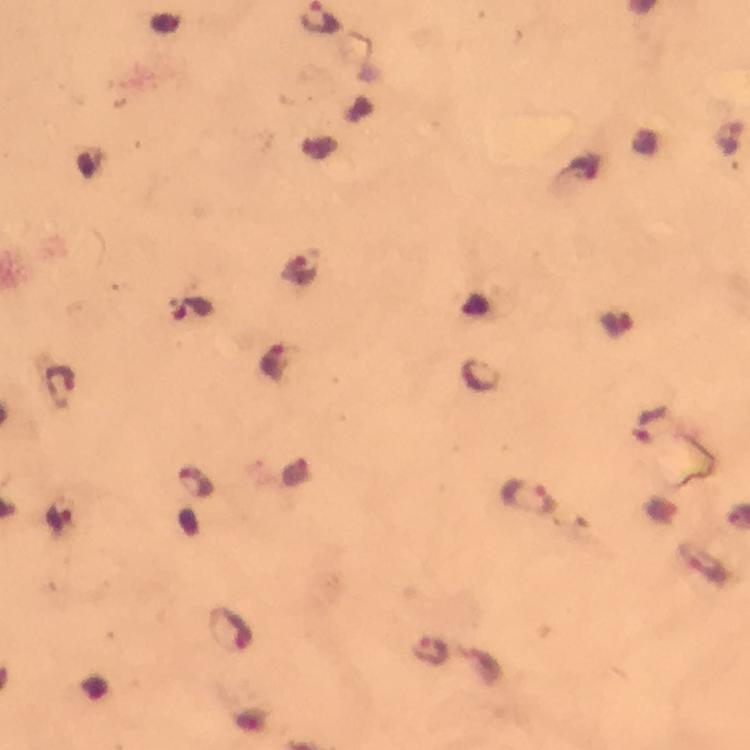

Approximate centers as [x, y] in pixels. Malaria parasite locations: [301, 266], [193, 306], [615, 324], [275, 360], [59, 385], [195, 482], [527, 498], [702, 563], [231, 628], [431, 649]. Cropped region of a single field of view. Image is 750×750 pixels. Giemsa-stained preparation. At 100x magnification. Thick blood smear. Photographed through the microscope with a smartphone camera. Immersion oil applied. From a malaria diagnostic workup.